Outline each blood parasite and name the species.
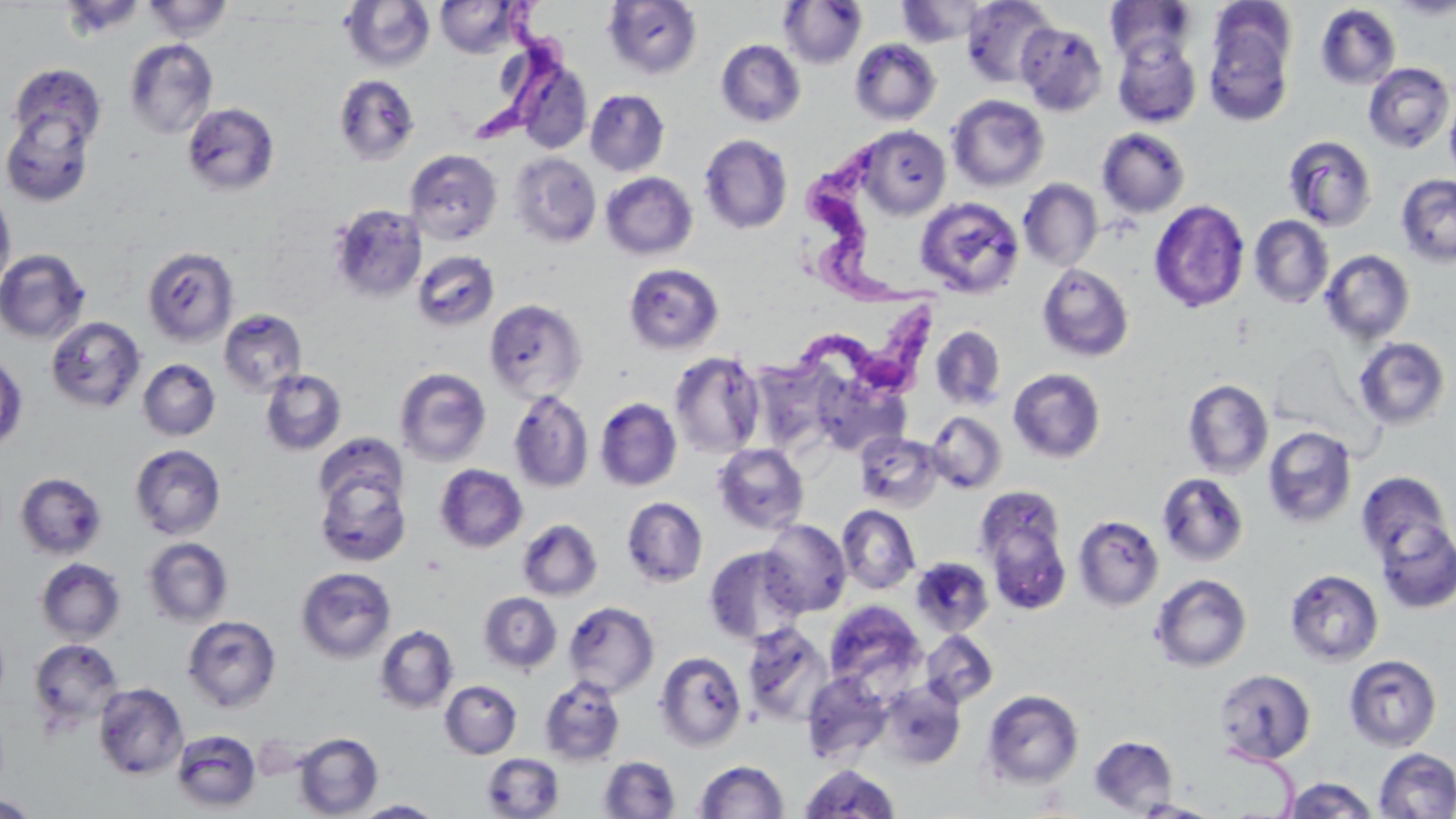

Approximate bounding boxes as [x1, y1, x2, y2] in pixels.
Trypanosoma brucei: [479, 0, 574, 149], [799, 143, 933, 298], [755, 301, 944, 404].
No Plasmodium falciparum, Plasmodium ovale, Plasmodium malariae, Plasmodium vivax, or Babesia divergens observed.

Uninfected red blood cell locations: [142, 0, 234, 41], [435, 0, 524, 58], [962, 0, 1058, 87], [1390, 0, 1456, 19], [341, 1, 435, 73], [603, 1, 702, 79], [778, 1, 868, 69], [896, 1, 990, 46], [1106, 1, 1197, 66], [1315, 3, 1401, 90], [1204, 5, 1297, 125], [1016, 21, 1107, 115], [1112, 37, 1202, 128], [124, 38, 218, 139], [716, 39, 806, 128], [849, 39, 941, 125], [516, 60, 593, 154], [7, 62, 107, 154], [1363, 62, 1454, 153], [333, 74, 420, 166], [585, 89, 669, 176], [947, 94, 1049, 192], [1444, 95, 1456, 178], [182, 102, 280, 197], [1, 106, 98, 207], [856, 126, 950, 219], [1097, 128, 1190, 218], [699, 134, 793, 235], [1282, 134, 1378, 231], [404, 149, 503, 246], [510, 153, 602, 248], [601, 172, 697, 260], [1396, 173, 1456, 267], [1019, 178, 1102, 271], [0, 186, 16, 293], [915, 196, 1025, 298], [1149, 199, 1250, 313], [328, 204, 427, 302], [1249, 215, 1334, 308], [142, 247, 239, 346], [0, 249, 90, 343], [412, 250, 500, 332], [1320, 250, 1415, 344], [623, 263, 724, 354], [1036, 263, 1135, 362], [484, 298, 586, 400], [219, 309, 307, 394], [46, 316, 146, 413], [931, 326, 1006, 411], [1352, 336, 1451, 431], [669, 351, 766, 458], [0, 352, 28, 451], [138, 358, 221, 441], [749, 358, 839, 454], [394, 367, 492, 467], [1008, 368, 1106, 462], [260, 369, 347, 456], [1183, 379, 1273, 479], [509, 389, 594, 493], [595, 398, 682, 491], [925, 410, 1007, 493], [1262, 426, 1357, 529], [854, 432, 944, 512], [312, 433, 407, 520], [712, 442, 809, 535], [129, 444, 226, 540], [314, 460, 412, 567], [434, 464, 528, 552], [1356, 471, 1452, 565], [15, 472, 107, 560], [1157, 472, 1249, 566], [975, 486, 1072, 610], [621, 496, 708, 587], [837, 505, 920, 594], [1073, 515, 1164, 611], [1372, 515, 1456, 614], [517, 518, 603, 601], [760, 519, 852, 616], [141, 537, 234, 627], [703, 546, 807, 645], [36, 557, 125, 645], [910, 557, 994, 637], [295, 566, 397, 664], [1285, 569, 1384, 666], [1150, 574, 1252, 672], [478, 592, 562, 675], [823, 600, 926, 693], [563, 601, 659, 697], [182, 615, 281, 713], [742, 621, 834, 726], [374, 625, 459, 714], [920, 630, 998, 708], [27, 638, 125, 732], [654, 650, 748, 752], [1344, 654, 1442, 752], [1214, 668, 1315, 765], [801, 672, 893, 765], [539, 676, 626, 766], [440, 680, 522, 759], [878, 680, 966, 770], [93, 682, 188, 780], [981, 689, 1084, 790], [172, 730, 261, 812], [293, 732, 383, 818], [1089, 735, 1178, 815], [1374, 748, 1456, 819], [481, 753, 564, 819], [598, 756, 680, 818], [694, 760, 788, 818], [800, 763, 899, 817], [1282, 777, 1378, 818], [0, 794, 39, 818], [354, 799, 444, 818], [1131, 800, 1222, 818]. Slide-level diagnosis: Trypanosoma brucei. Light microscopy. Single field of view. May-Grünwald-Giemsa stain. Thin blood smear. Image is 1456×819 pixels. 1000x magnification.